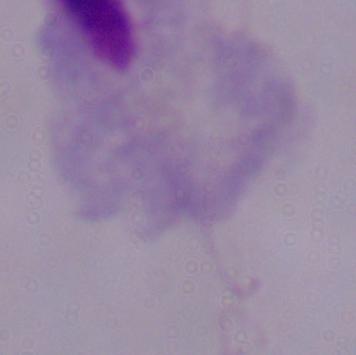
modality: photomicrograph
identification: trichomonad
magnification: 1000x